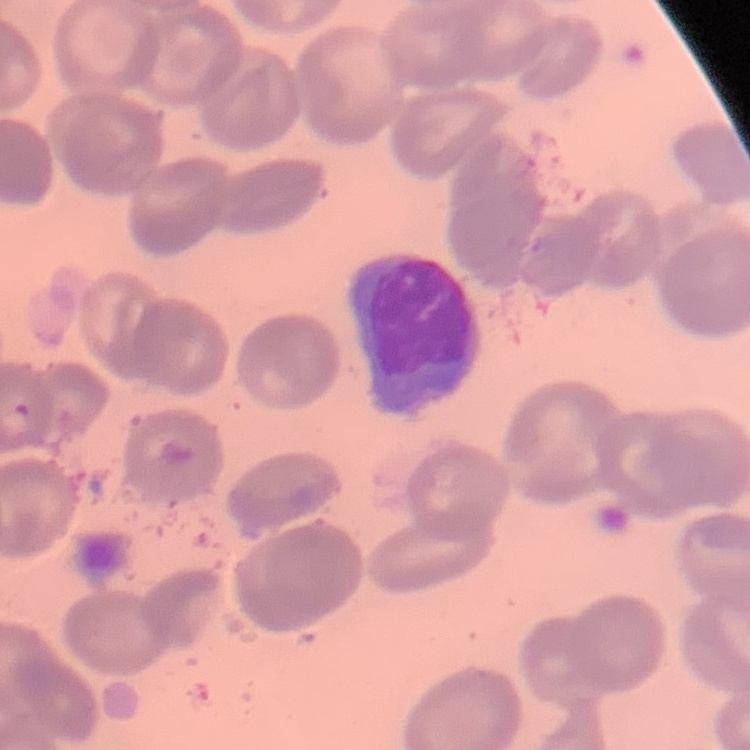

Summary:
  - Red blood cell morphology: no rouleaux formation
  - Preparation: thin blood smear
  - Image type: one tile cut from a larger photomicrograph
  - Stain: Field's or Giemsa